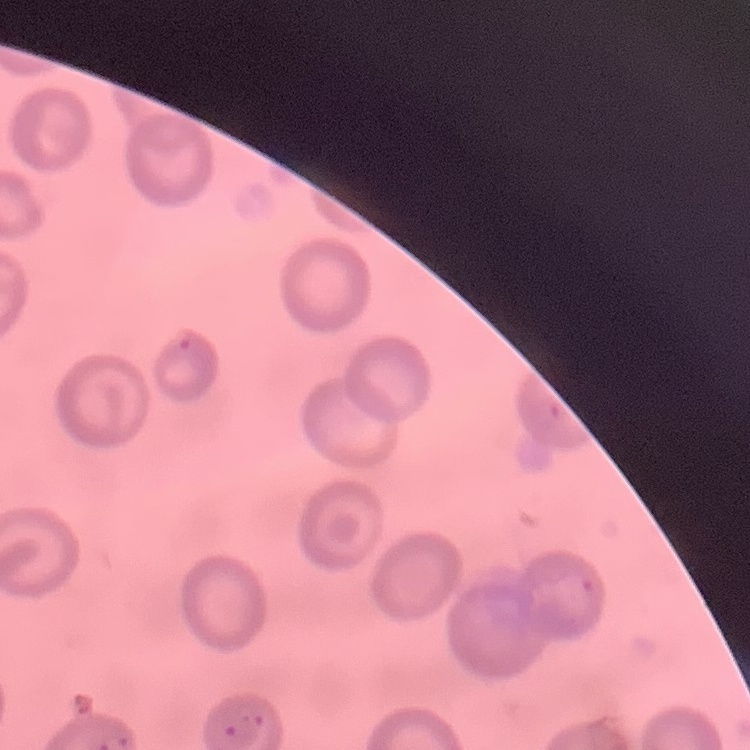 The red blood cells exhibit no rouleaux formation. Stained with either Field's or Giemsa. Thin peripheral smear. One tile cut from a larger photomicrograph.